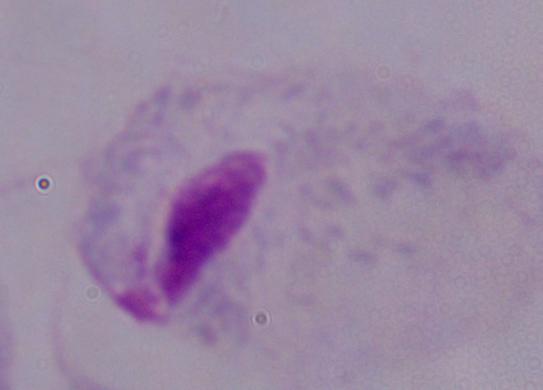

magnification = 1000x
identification = trichomonad
modality = photomicrograph